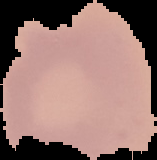

Malaria status: uninfected. From a thin blood film. Image is 157×160 pixels. The area outside the segmented cell region is set to black.